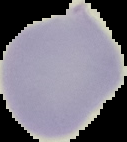
image size = 127×142 pixels
preparation = thin blood film
result = no malaria parasites detected
image type = segmented cell region on a black background